Assess for malaria.
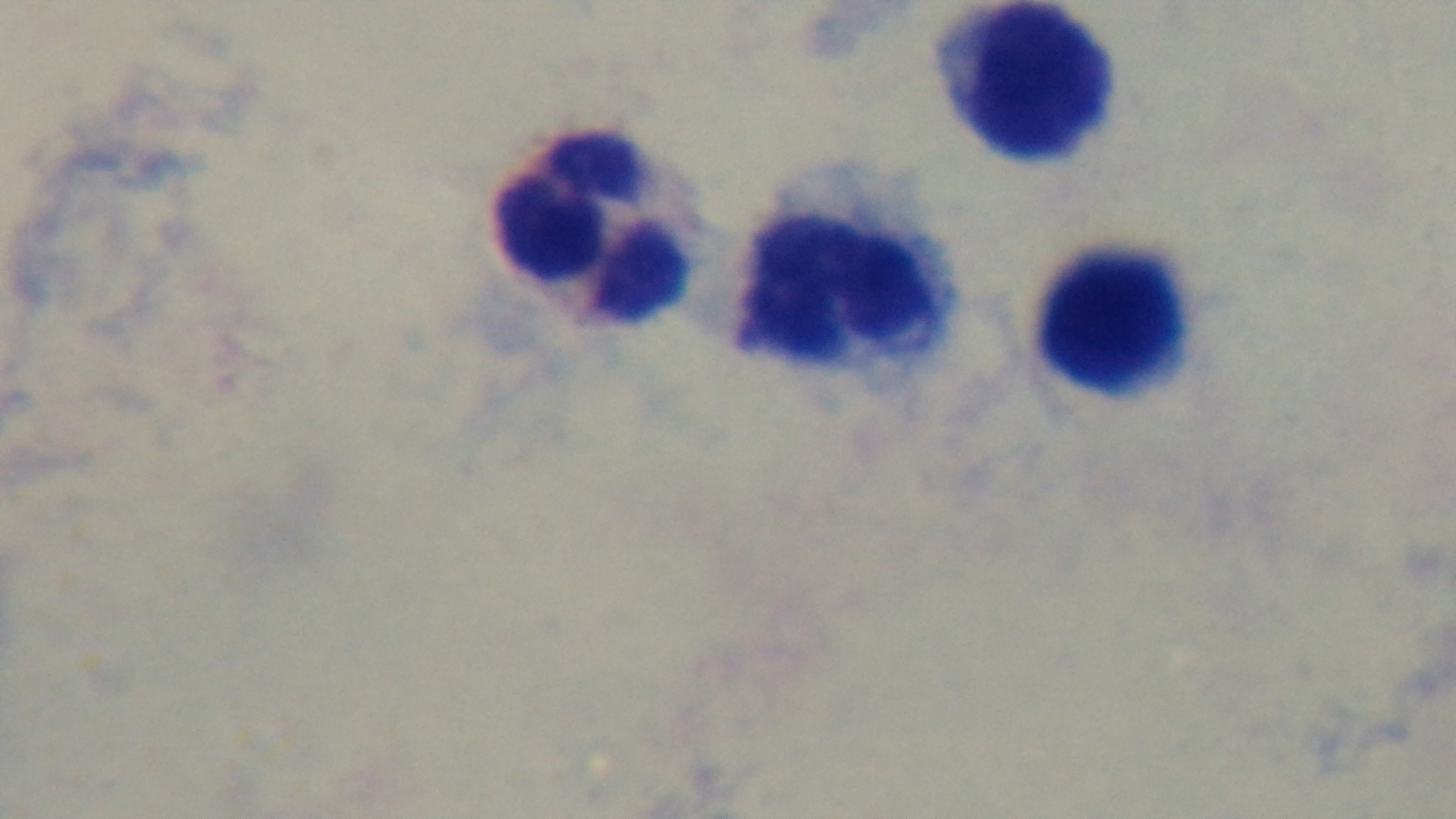
Uninfected.

objective = 100x oil immersion
modality = light microscopy
field of view = single
stain = Giemsa
preparation = thick smear
capture = mounted 4K digital camera